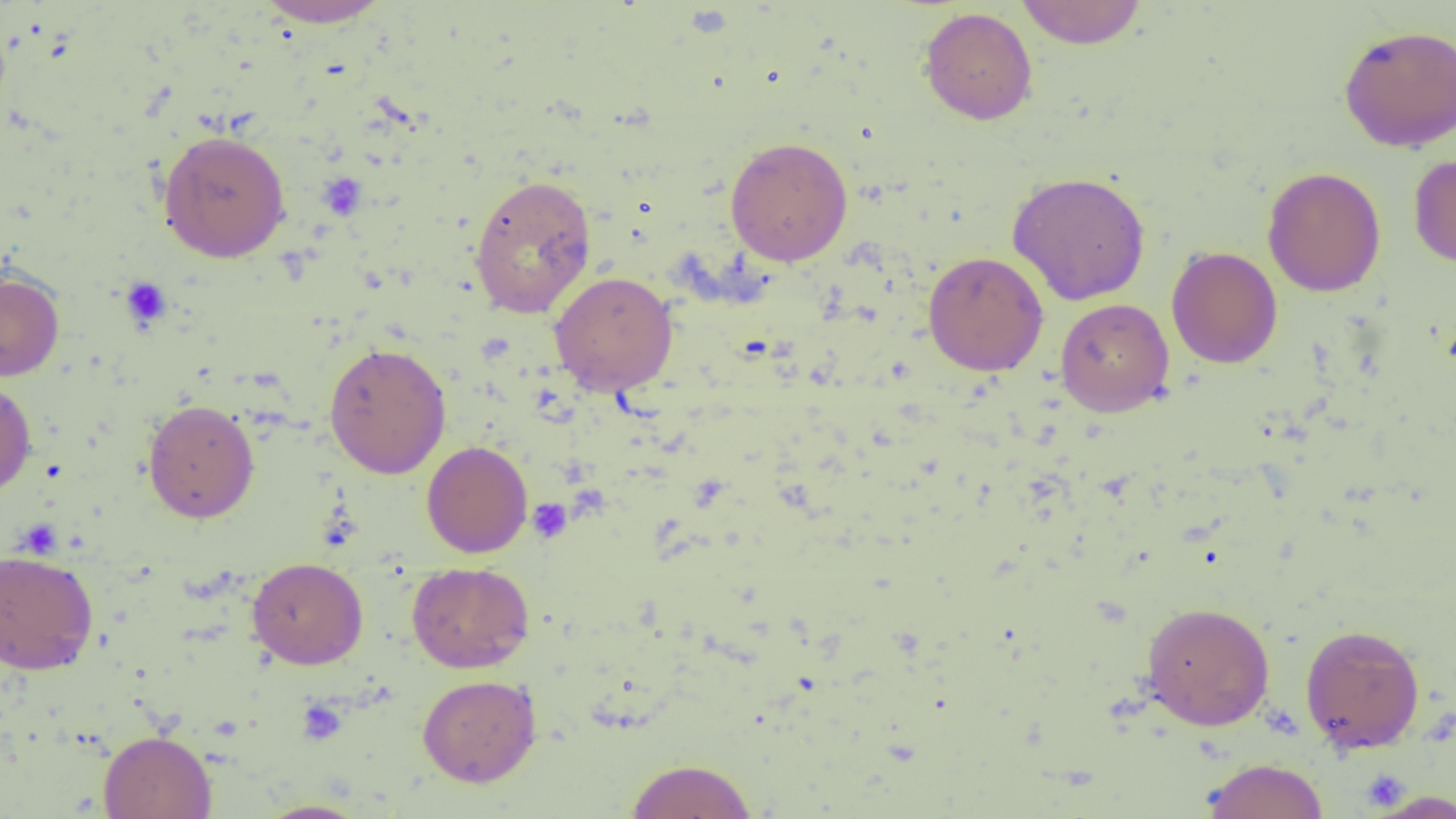

slide-level diagnosis = negative for blood parasites
modality = optical microscopy
uninfected red blood cell locations = approximate bounding boxes as (x1,y1)-(x2,y2) corner pairs in pixels: (254,0)-(395,28), (1015,0)-(1148,49), (919,7)-(1037,125), (1338,24)-(1456,152), (157,130)-(291,262), (725,136)-(853,267), (1408,152)-(1456,268), (1262,167)-(1386,296), (1007,171)-(1151,305), (468,173)-(597,318), (1167,246)-(1283,369), (923,251)-(1048,376), (0,270)-(65,381), (550,272)-(678,395), (1055,298)-(1174,417), (323,342)-(452,478), (0,377)-(36,497), (143,399)-(260,524), (421,441)-(532,558), (0,549)-(98,675), (247,557)-(368,669), (406,562)-(534,673), (1141,601)-(1275,730), (1299,623)-(1426,753), (417,674)-(541,787), (98,730)-(216,819), (1201,757)-(1329,819), (624,758)-(758,818), (1363,788)-(1456,818), (254,799)-(372,818)
field of view = single
preparation = thin blood film
magnification = 1000x
image size = 1456×819 pixels
platelet locations = approximate bounding boxes as (x1,y1)-(x2,y2) corner pairs in pixels: (120,276)-(172,329), (527,498)-(572,542), (296,698)-(347,745)